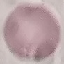

Summary:
  - Malaria status: uninfected
  - Preparation: thin blood film
  - Image type: automatically extracted cell patch, resized to 64 × 64 pixels
  - Stain: Giemsa
  - Capture: smartphone through the microscope eyepiece